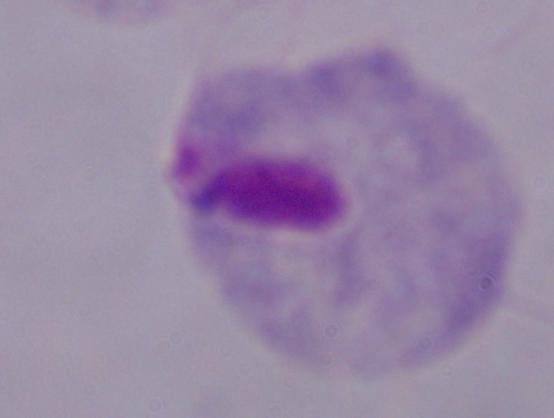
identification = trichomonad
magnification = 1000x
modality = photomicrograph